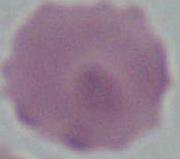

identification = erythrocyte
magnification = 1000x
modality = micrograph